Identify the parasite.
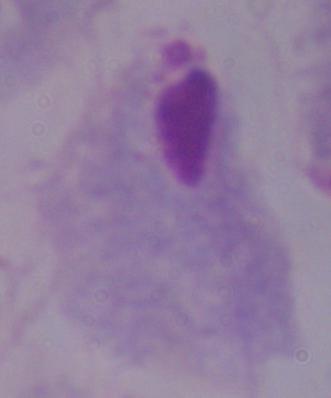

This is a trichomonad.

1000x magnification. Micrograph.